Classify this cell by malaria status.
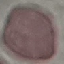

It is uninfected.

Automatically extracted cell patch, resized to 64 × 64 pixels. Thin blood smear. Acquired by smartphone through the microscope eyepiece. Giemsa stain.